Give the position of every Plasmodium parasite visible.
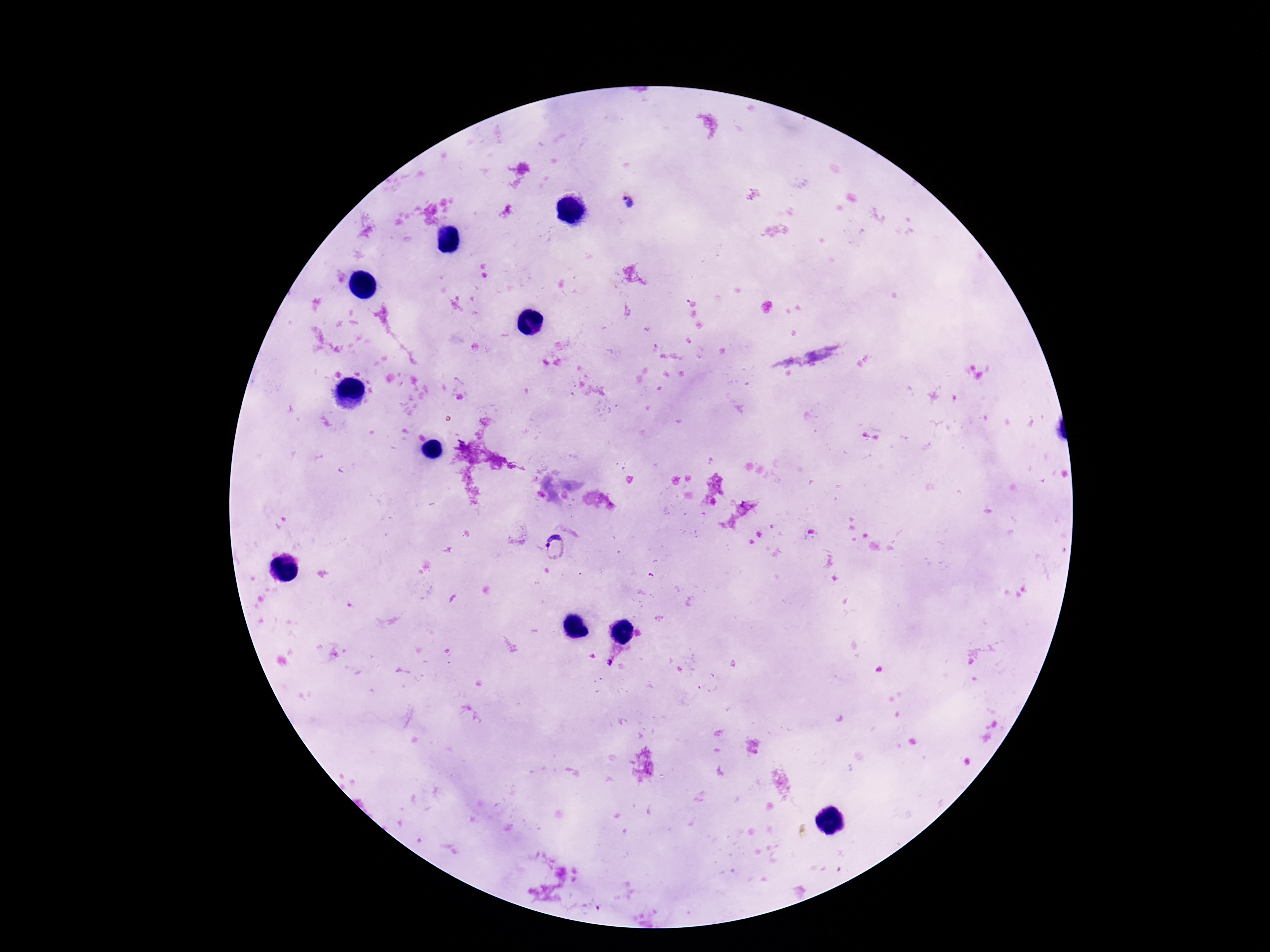

Approximate object centers, in pixels from the top-left corner.
Plasmodium parasites: (x=627, y=203), (x=557, y=549), (x=609, y=662).

Summary:
  - Image size: 1270×952 pixels
  - Stain: Giemsa
  - Preparation: thick blood film
  - Patient malaria status: infected
  - Magnification: 100x
  - Field of view: single
  - Capture: smartphone camera through the microscope eyepiece